Give the extent of all Babesia divergens-infected red blood cells.
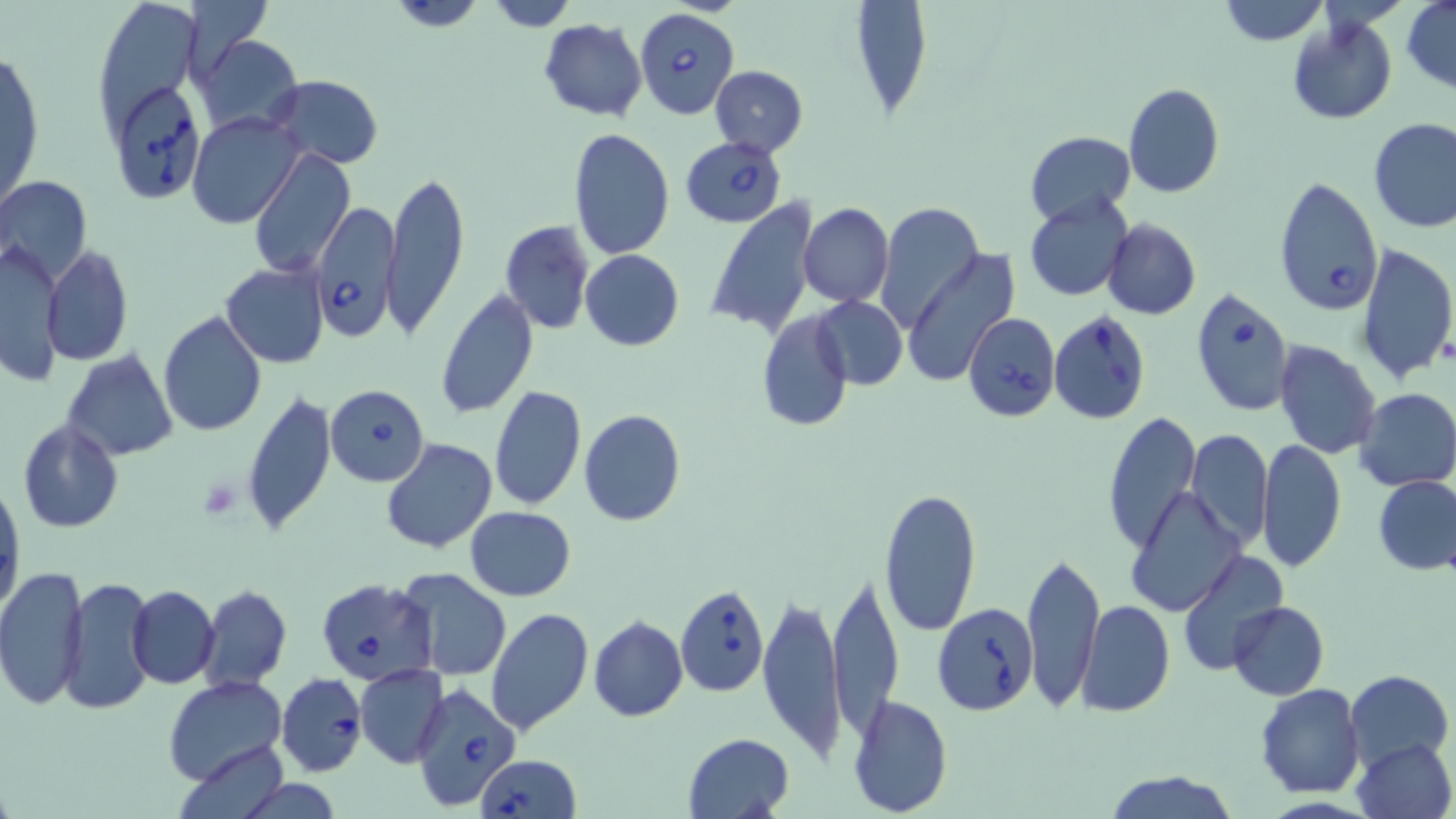

Approximate bounding boxes as named x1/y1/x2/y2 corners in pixels.
Babesia divergens-infected red blood cells: (x1=634, y1=8, x2=739, y2=119), (x1=116, y1=85, x2=204, y2=207), (x1=682, y1=138, x2=786, y2=227), (x1=1273, y1=176, x2=1384, y2=316), (x1=311, y1=202, x2=403, y2=342), (x1=1190, y1=288, x2=1294, y2=416), (x1=1049, y1=308, x2=1151, y2=423), (x1=962, y1=313, x2=1060, y2=422), (x1=326, y1=384, x2=429, y2=486), (x1=315, y1=578, x2=438, y2=687), (x1=675, y1=585, x2=770, y2=696), (x1=932, y1=600, x2=1038, y2=714), (x1=277, y1=672, x2=368, y2=777), (x1=409, y1=684, x2=520, y2=810), (x1=475, y1=755, x2=581, y2=819).

Summary:
  - Uninfected red blood cell locations: (x1=384, y1=0, x2=493, y2=31), (x1=482, y1=0, x2=581, y2=30), (x1=851, y1=0, x2=934, y2=113), (x1=1219, y1=0, x2=1328, y2=46), (x1=1402, y1=1, x2=1456, y2=91), (x1=100, y1=3, x2=202, y2=142), (x1=1286, y1=18, x2=1396, y2=124), (x1=538, y1=19, x2=648, y2=120), (x1=195, y1=36, x2=302, y2=136), (x1=1, y1=44, x2=43, y2=218), (x1=710, y1=65, x2=809, y2=158), (x1=269, y1=75, x2=381, y2=169), (x1=1122, y1=84, x2=1223, y2=198), (x1=187, y1=111, x2=304, y2=228), (x1=1368, y1=118, x2=1456, y2=233), (x1=567, y1=129, x2=676, y2=260), (x1=1024, y1=129, x2=1135, y2=225), (x1=248, y1=148, x2=354, y2=279), (x1=382, y1=168, x2=469, y2=342), (x1=0, y1=176, x2=93, y2=286), (x1=1023, y1=193, x2=1134, y2=302), (x1=704, y1=200, x2=820, y2=339), (x1=798, y1=203, x2=894, y2=308), (x1=877, y1=203, x2=984, y2=336), (x1=1102, y1=218, x2=1200, y2=321), (x1=499, y1=220, x2=595, y2=335), (x1=4, y1=236, x2=65, y2=390), (x1=1356, y1=242, x2=1456, y2=385), (x1=42, y1=246, x2=133, y2=368), (x1=899, y1=247, x2=1021, y2=389), (x1=579, y1=250, x2=685, y2=351), (x1=221, y1=263, x2=329, y2=368), (x1=435, y1=292, x2=538, y2=420), (x1=813, y1=297, x2=907, y2=390), (x1=755, y1=310, x2=852, y2=429), (x1=159, y1=311, x2=266, y2=437), (x1=1273, y1=340, x2=1384, y2=460), (x1=60, y1=350, x2=179, y2=462), (x1=489, y1=385, x2=586, y2=512), (x1=1355, y1=387, x2=1456, y2=493), (x1=242, y1=390, x2=337, y2=538), (x1=578, y1=410, x2=687, y2=527), (x1=1101, y1=411, x2=1202, y2=553), (x1=16, y1=419, x2=123, y2=534), (x1=1188, y1=429, x2=1274, y2=549), (x1=1256, y1=438, x2=1347, y2=573), (x1=381, y1=439, x2=497, y2=555), (x1=1373, y1=475, x2=1456, y2=576), (x1=1, y1=479, x2=23, y2=613), (x1=878, y1=487, x2=983, y2=638), (x1=1125, y1=487, x2=1248, y2=618), (x1=465, y1=506, x2=576, y2=600), (x1=1022, y1=549, x2=1103, y2=712), (x1=1177, y1=550, x2=1289, y2=675), (x1=0, y1=565, x2=89, y2=710), (x1=396, y1=567, x2=512, y2=680), (x1=828, y1=571, x2=904, y2=736), (x1=59, y1=575, x2=157, y2=715), (x1=126, y1=584, x2=219, y2=688), (x1=198, y1=584, x2=292, y2=691), (x1=758, y1=584, x2=847, y2=764), (x1=1075, y1=600, x2=1174, y2=718), (x1=1229, y1=601, x2=1328, y2=700), (x1=485, y1=607, x2=593, y2=737), (x1=589, y1=616, x2=688, y2=722), (x1=355, y1=663, x2=450, y2=767), (x1=1346, y1=669, x2=1453, y2=768), (x1=163, y1=676, x2=289, y2=788), (x1=1255, y1=684, x2=1365, y2=798), (x1=847, y1=694, x2=953, y2=818), (x1=681, y1=733, x2=797, y2=819), (x1=1352, y1=737, x2=1455, y2=819), (x1=178, y1=741, x2=290, y2=819), (x1=1103, y1=768, x2=1237, y2=819)
  - Slide-level diagnosis: Babesia divergens
  - Modality: optical microscopy
  - Magnification: 1000x
  - Field of view: one of a larger specimen
  - Stain: May-Grünwald-Giemsa
  - Preparation: thin blood smear
  - Image size: 1456×819 pixels